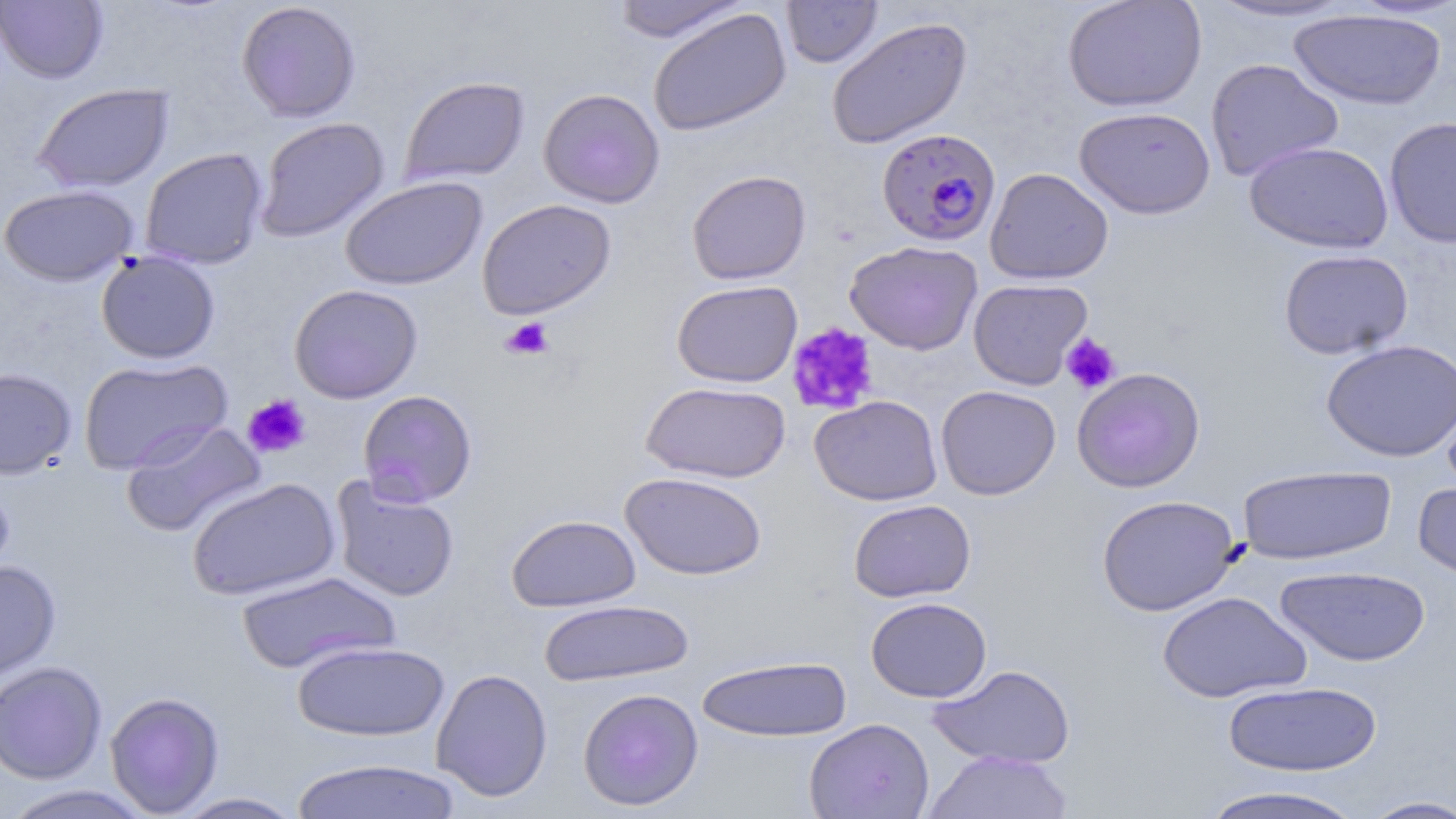

Summary:
  - Coordinate format: approximate bounding boxes as named x1/y1/x2/y2 corners in pixels
  - Platelet locations: (x1=500, y1=317, x2=555, y2=360), (x1=786, y1=323, x2=878, y2=416), (x1=1061, y1=333, x2=1121, y2=394), (x1=243, y1=394, x2=311, y2=459)
  - Plasmodium falciparum-infected red blood cell locations: (x1=877, y1=127, x2=1001, y2=247)
  - Uninfected red blood cell locations: (x1=0, y1=0, x2=108, y2=84), (x1=780, y1=0, x2=883, y2=68), (x1=1063, y1=0, x2=1207, y2=112), (x1=1201, y1=0, x2=1358, y2=23), (x1=610, y1=1, x2=751, y2=43), (x1=236, y1=2, x2=362, y2=122), (x1=646, y1=8, x2=792, y2=136), (x1=1288, y1=8, x2=1446, y2=110), (x1=826, y1=16, x2=973, y2=150), (x1=1205, y1=58, x2=1344, y2=181), (x1=399, y1=76, x2=529, y2=186), (x1=32, y1=82, x2=173, y2=193), (x1=538, y1=87, x2=665, y2=208), (x1=1218, y1=90, x2=1368, y2=230), (x1=1074, y1=106, x2=1216, y2=219), (x1=1384, y1=116, x2=1456, y2=248), (x1=254, y1=117, x2=390, y2=242), (x1=1244, y1=140, x2=1394, y2=253), (x1=140, y1=148, x2=269, y2=269), (x1=985, y1=168, x2=1113, y2=285), (x1=686, y1=169, x2=811, y2=285), (x1=341, y1=176, x2=487, y2=290), (x1=0, y1=184, x2=138, y2=287), (x1=477, y1=198, x2=617, y2=319), (x1=845, y1=240, x2=983, y2=355), (x1=1278, y1=249, x2=1414, y2=360), (x1=96, y1=250, x2=221, y2=364), (x1=968, y1=278, x2=1093, y2=390), (x1=671, y1=279, x2=802, y2=388), (x1=288, y1=284, x2=423, y2=404), (x1=1321, y1=339, x2=1456, y2=462), (x1=78, y1=356, x2=232, y2=475), (x1=1071, y1=367, x2=1205, y2=492), (x1=0, y1=368, x2=77, y2=479), (x1=640, y1=381, x2=790, y2=484), (x1=935, y1=385, x2=1061, y2=500), (x1=357, y1=389, x2=478, y2=507), (x1=809, y1=394, x2=943, y2=506), (x1=121, y1=419, x2=265, y2=537), (x1=1237, y1=464, x2=1396, y2=565), (x1=620, y1=471, x2=767, y2=580), (x1=0, y1=475, x2=15, y2=586), (x1=330, y1=476, x2=460, y2=602), (x1=186, y1=477, x2=341, y2=601), (x1=1413, y1=478, x2=1456, y2=585), (x1=1096, y1=494, x2=1242, y2=616), (x1=848, y1=499, x2=976, y2=602), (x1=506, y1=514, x2=641, y2=612), (x1=0, y1=560, x2=61, y2=686), (x1=1274, y1=565, x2=1431, y2=667), (x1=236, y1=571, x2=399, y2=675), (x1=1157, y1=591, x2=1311, y2=703), (x1=866, y1=597, x2=991, y2=702), (x1=539, y1=598, x2=694, y2=687), (x1=291, y1=640, x2=450, y2=742), (x1=697, y1=655, x2=852, y2=742), (x1=0, y1=660, x2=107, y2=784), (x1=928, y1=664, x2=1075, y2=769), (x1=431, y1=668, x2=553, y2=802), (x1=1222, y1=681, x2=1383, y2=777), (x1=577, y1=687, x2=704, y2=811), (x1=105, y1=691, x2=225, y2=817), (x1=804, y1=717, x2=934, y2=819), (x1=923, y1=750, x2=1073, y2=819), (x1=290, y1=757, x2=464, y2=818), (x1=1194, y1=784, x2=1368, y2=819), (x1=1, y1=785, x2=152, y2=818), (x1=171, y1=792, x2=307, y2=818), (x1=1359, y1=795, x2=1456, y2=818)
  - Slide-level diagnosis: Plasmodium falciparum
  - Image size: 1456×819 pixels
  - Modality: light microscopy
  - Preparation: thin blood smear
  - Stain: May-Grünwald-Giemsa
  - Field of view: one of a larger specimen
  - Magnification: 1000x